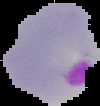
image_type: cell region segmented out of the field of view; surrounding area masked to black
result: malaria parasites detected
preparation: thin blood smear
image_size: 100×106 pixels